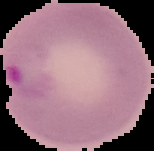 From a thin blood film. Image is 154×151 pixels. Cell region segmented out of the field of view; the surrounding area is masked to black. Result: malaria parasites identified.